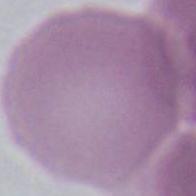
Summary:
  - Identification: erythrocyte
  - Magnification: 1000x
  - Modality: micrograph